State which parasite is depicted.
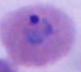

This is Plasmodium.

Summary:
  - Magnification: 400x or 1000x
  - Modality: photomicrograph